Report the malaria status of this cell.
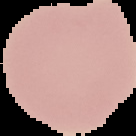

It is uninfected.

Image is 136×136 pixels. The area outside the segmented cell region is set to black. From a thin blood film.